Classify this cell by malaria status.
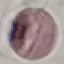
It is uninfected.

preparation: thin blood smear
image_type: cell patch, automatically extracted from a larger field of view and resized to 64 × 64 pixels
capture: smartphone camera at the microscope eyepiece
stain: Giemsa